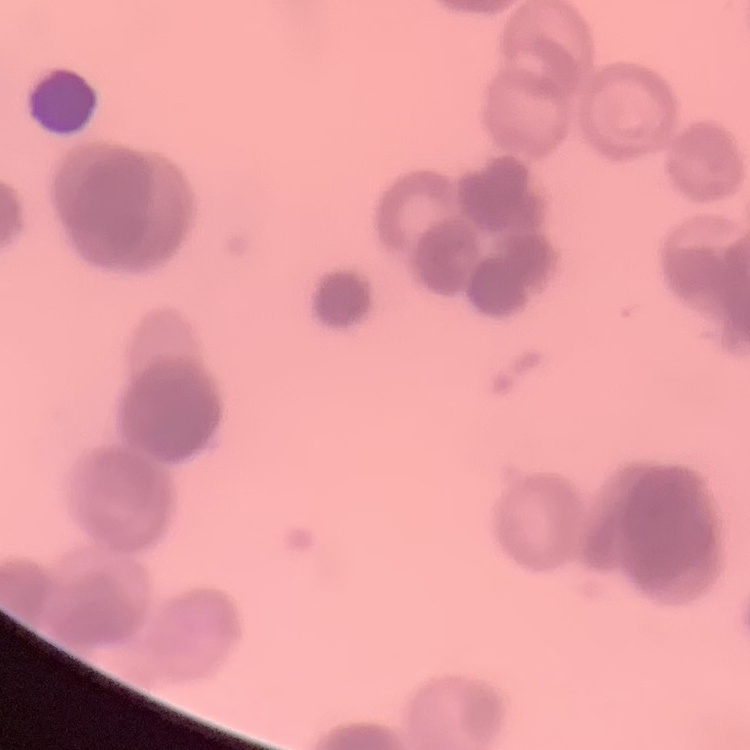
erythrocyte_morphology: rouleaux formation
preparation: thin peripheral smear
stain: Field's or Giemsa
image_type: one tile cut from a larger photomicrograph